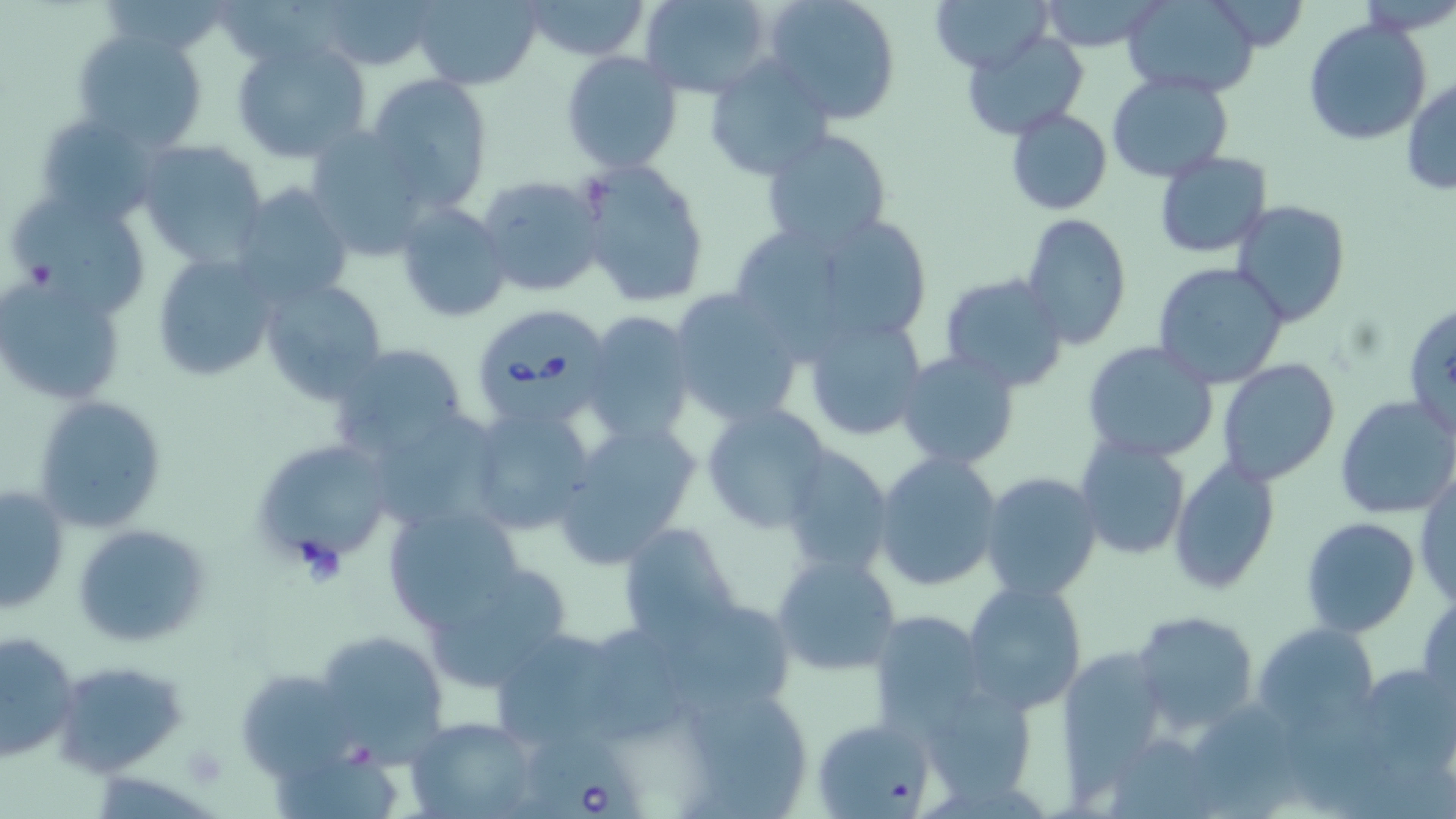

Approximate bounding boxes as [x1, y1, x2, y2] in pixels. Platelet locations: [181, 741, 231, 789]. Uninfected red blood cell locations: [320, 0, 437, 72], [409, 0, 543, 90], [522, 0, 651, 61], [642, 0, 776, 99], [762, 0, 902, 125], [929, 0, 1051, 73], [1037, 0, 1167, 53], [1122, 0, 1261, 97], [1304, 17, 1431, 144], [73, 28, 209, 153], [961, 31, 1090, 140], [230, 38, 373, 164], [560, 50, 684, 174], [702, 53, 838, 182], [1106, 72, 1235, 183], [366, 73, 494, 212], [1402, 77, 1455, 195], [1006, 107, 1112, 216], [33, 110, 162, 226], [303, 127, 437, 261], [759, 129, 893, 251], [135, 140, 269, 267], [1154, 149, 1272, 259], [578, 162, 709, 308], [475, 173, 607, 299], [231, 180, 355, 309], [10, 193, 154, 316], [394, 199, 513, 324], [1231, 201, 1352, 326], [746, 207, 936, 355], [1020, 213, 1133, 351], [959, 243, 1119, 376], [151, 250, 279, 383], [1153, 261, 1290, 388], [938, 272, 1069, 392], [2, 276, 126, 403], [257, 276, 391, 404], [668, 287, 808, 428], [1402, 299, 1456, 444], [581, 312, 697, 444], [801, 313, 929, 440], [1082, 341, 1218, 463], [325, 343, 475, 464], [895, 349, 1022, 472], [1216, 358, 1342, 486], [31, 394, 166, 534], [1335, 394, 1455, 520], [466, 401, 597, 535], [700, 401, 833, 533], [366, 407, 503, 531], [550, 419, 702, 566], [1072, 435, 1191, 562], [249, 439, 393, 570], [777, 447, 899, 578], [872, 451, 1005, 593], [1169, 457, 1280, 593], [980, 472, 1102, 601], [1415, 473, 1455, 607], [1, 484, 70, 612], [382, 503, 524, 633], [1301, 517, 1420, 638], [619, 521, 740, 646], [72, 522, 209, 649], [771, 554, 902, 677], [423, 562, 575, 691], [962, 580, 1088, 715], [1417, 592, 1456, 712], [1129, 609, 1259, 735], [868, 611, 992, 738], [1255, 623, 1382, 738], [484, 624, 635, 751], [0, 629, 81, 763], [314, 629, 450, 763], [1057, 642, 1173, 787], [51, 658, 189, 777], [236, 665, 359, 777], [1356, 667, 1453, 780], [918, 681, 1041, 807], [674, 683, 817, 817], [405, 716, 541, 819], [813, 717, 936, 819]. Babesia divergens-infected red blood cell locations: [469, 303, 613, 431], [528, 729, 648, 819]. Slide-level diagnosis: Babesia divergens. Thin blood smear. Image is 1456×819 pixels. Light microscopy. May-Grünwald-Giemsa-stained preparation. Single field of view. Captured at 1000x magnification.